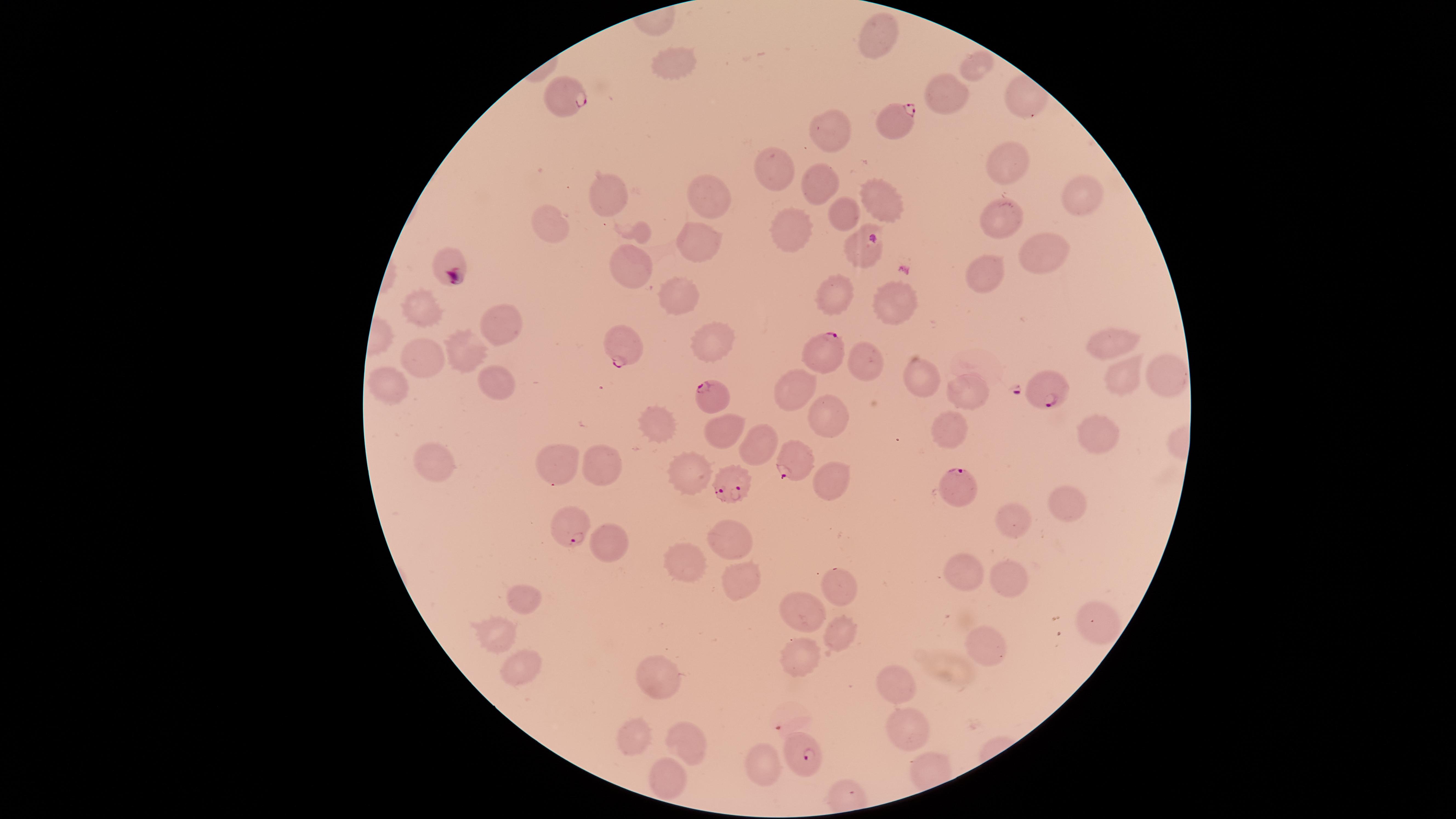

Approximate marker points as {x, y} in pixels.
Summary:
  - Uninfected RBCs: {881, 33}, {671, 62}, {975, 68}, {948, 93}, {830, 127}, {1006, 163}, {772, 170}, {818, 180}, {607, 193}, {1078, 194}, {709, 200}, {882, 201}, {1001, 210}, {841, 212}, {553, 226}, {638, 232}, {790, 233}, {860, 246}, {694, 247}, {1041, 254}, {446, 260}, {631, 264}, {985, 274}, {681, 296}, {830, 296}, {894, 306}, {419, 310}, {505, 322}, {1108, 342}, {712, 345}, {466, 351}, {865, 356}, {426, 357}, {1168, 373}, {923, 375}, {1110, 377}, {385, 383}, {492, 383}, {794, 388}, {968, 389}, {829, 418}, {654, 424}, {710, 430}, {946, 430}, {1095, 430}, {755, 444}, {430, 458}, {603, 461}, {559, 462}, {687, 478}, {830, 480}, {1064, 507}, {1011, 516}, {726, 533}, {600, 545}, {969, 569}, {680, 570}, {740, 579}, {1011, 582}, {840, 590}, {523, 594}, {799, 608}, {1099, 620}, {839, 629}, {493, 636}, {988, 648}, {797, 657}, {517, 661}, {899, 680}, {652, 684}, {909, 721}, {628, 733}, {688, 734}, {761, 767}, {664, 784}
  - Parasitized RBCs: {564, 96}, {896, 122}, {623, 344}, {828, 350}, {1044, 387}, {712, 395}, {793, 463}, {953, 481}, {724, 483}, {569, 527}, {807, 752}
  - Presence: malaria parasites identified
  - Capture: smartphone photograph through the microscope eyepiece
  - Species: Plasmodium falciparum
  - Field of view: single
  - Preparation: thin blood smear
  - Stain: Giemsa
  - Image size: 1456×819 pixels
  - Visible region: circular